Identify the parasite.
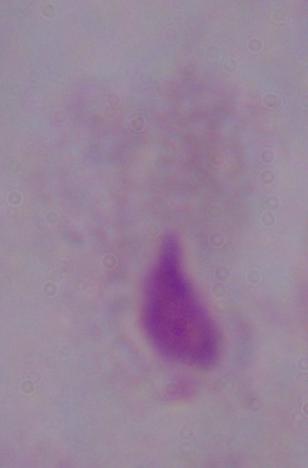
A trichomonad.

Captured at 1000x magnification. Micrograph.